Name the parasite shown.
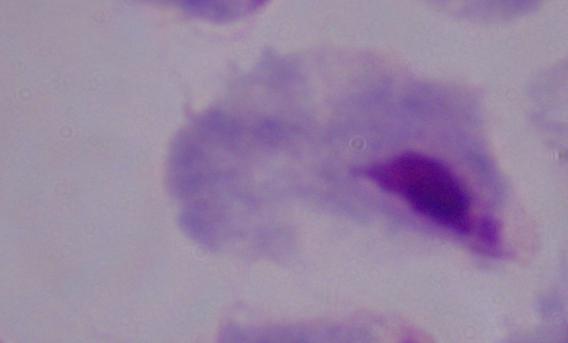
This is a trichomonad.

Photomicrograph. 1000x magnification.